Comment on the morphology of the red blood cells.
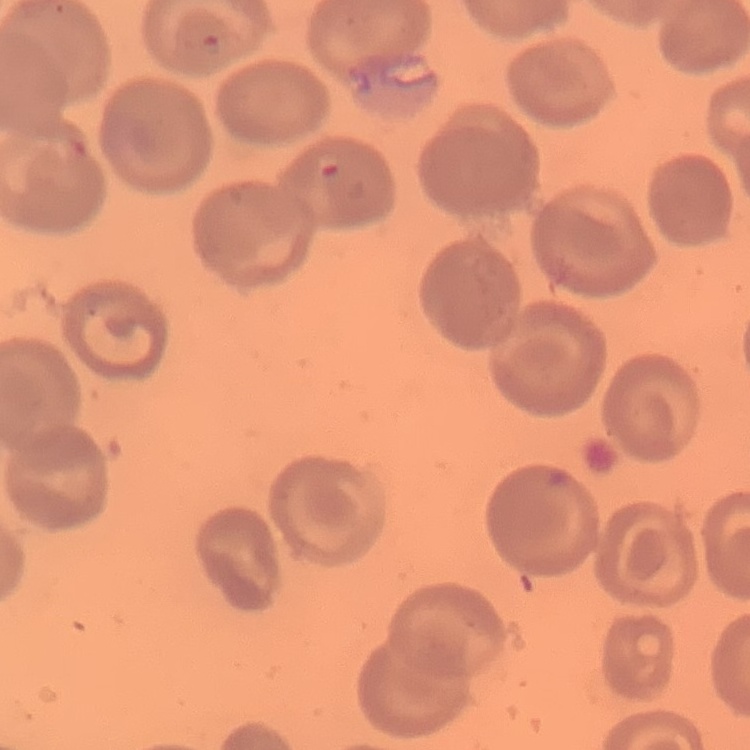
No rouleaux formation.

Thin peripheral smear. One tile cut from a larger photomicrograph. Field's or Giemsa stain.